State which parasite is depicted.
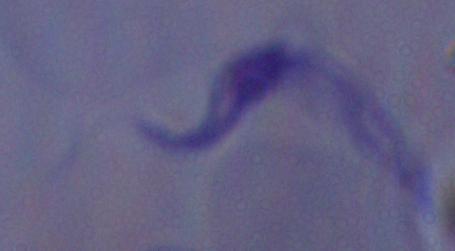

A trypanosome.

modality = micrograph
magnification = 1000x